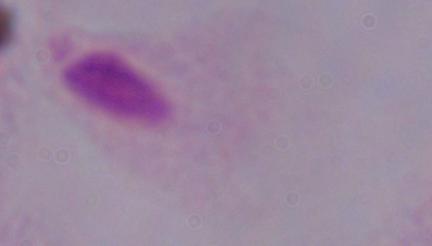

Summary:
  - Identification: trichomonad
  - Magnification: 1000x
  - Modality: photomicrograph